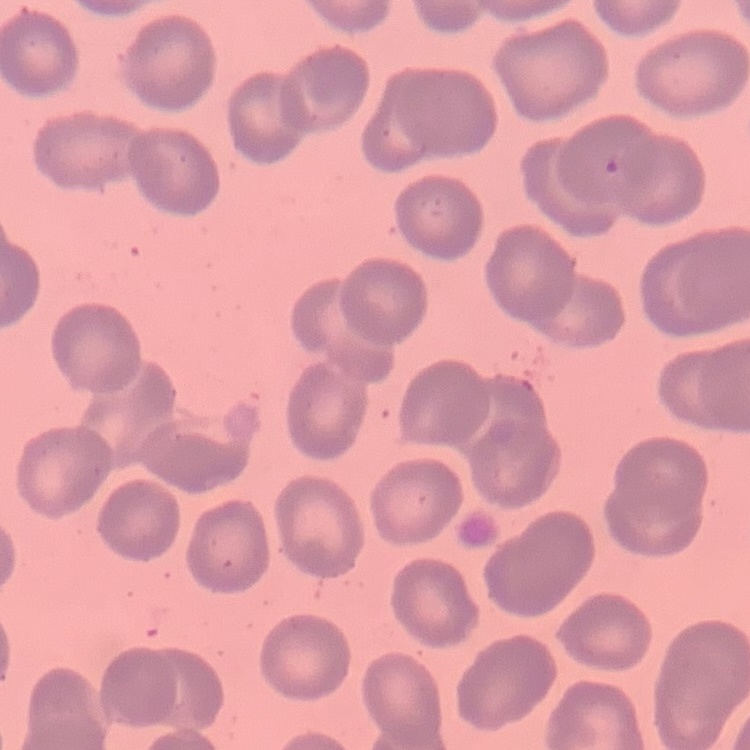 The erythrocytes exhibit no rouleaux formation. Thin blood film. Stained with either Field's or Giemsa. Square crop of a larger photomicrograph.